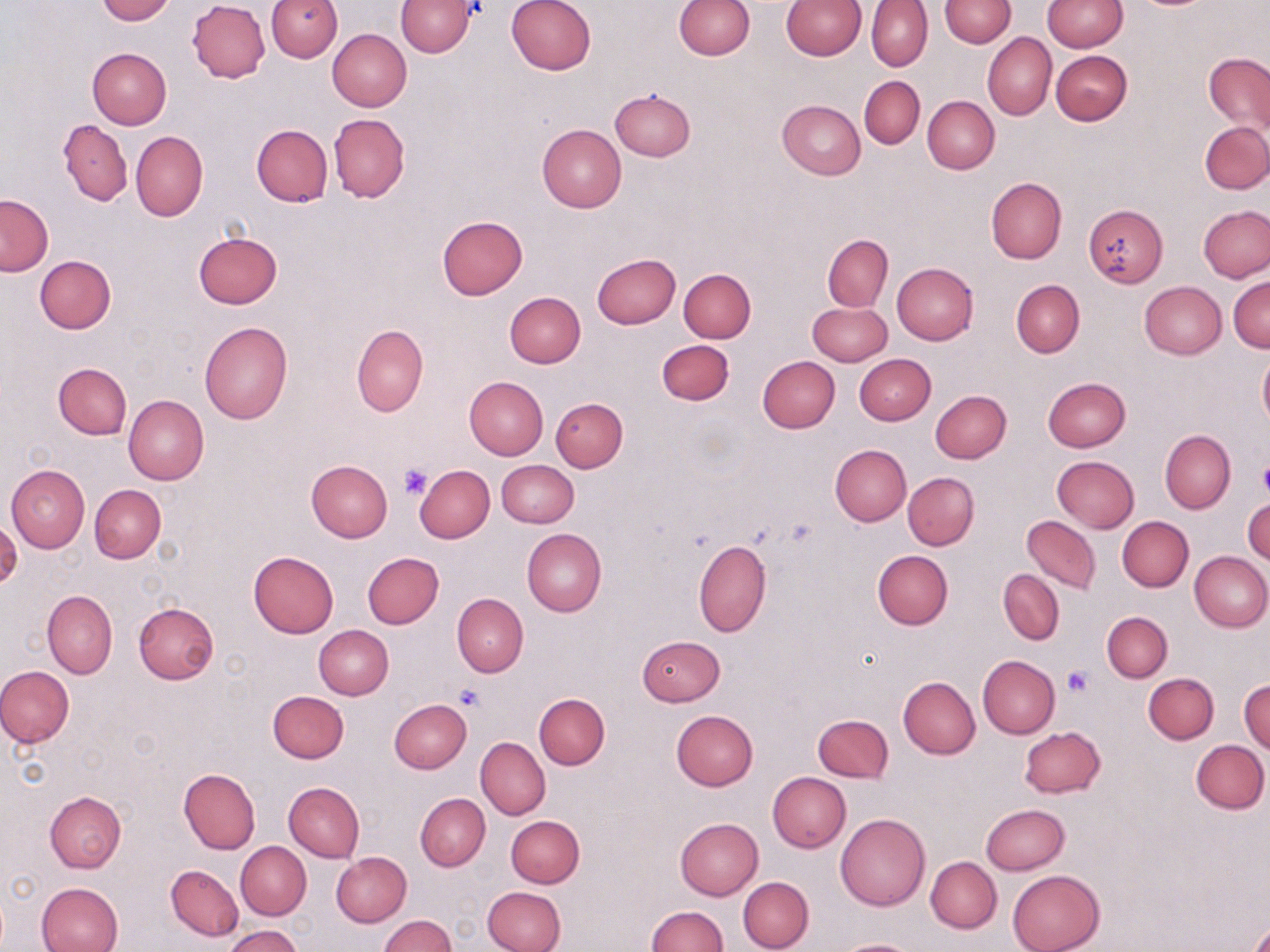

Approximate bounding boxes as (x1, y1, x2, y2) in pixels. Platelet locations: (1257, 459, 1270, 497), (399, 462, 433, 499), (1063, 664, 1094, 696), (455, 684, 485, 711). Uninfected red blood cell locations: (96, 0, 173, 24), (266, 0, 342, 62), (505, 0, 596, 75), (674, 0, 754, 59), (781, 0, 864, 59), (939, 0, 1015, 47), (1041, 0, 1128, 51), (187, 1, 270, 82), (397, 1, 475, 57), (867, 1, 932, 71), (327, 28, 411, 111), (983, 32, 1056, 119), (88, 48, 171, 128), (1051, 50, 1132, 126), (1204, 53, 1270, 134), (859, 76, 924, 149), (610, 88, 695, 161), (923, 95, 999, 174), (777, 99, 865, 179), (329, 114, 410, 202), (58, 119, 131, 206), (1201, 122, 1270, 193), (251, 123, 333, 206), (537, 123, 627, 212), (131, 131, 208, 220), (986, 177, 1067, 263), (0, 194, 53, 276), (1082, 204, 1167, 287), (1197, 205, 1270, 283), (437, 215, 527, 299), (193, 231, 283, 309), (823, 235, 892, 311), (593, 253, 680, 328), (35, 256, 116, 334), (892, 262, 978, 344), (679, 269, 755, 342), (1228, 275, 1269, 352), (1011, 280, 1083, 355), (1140, 281, 1226, 360), (504, 291, 585, 368), (807, 302, 891, 366), (199, 321, 294, 424), (352, 324, 428, 415), (656, 340, 734, 405), (1257, 353, 1270, 431), (853, 354, 935, 424), (757, 356, 840, 433), (53, 363, 132, 439), (464, 376, 548, 460), (1042, 377, 1131, 451), (931, 390, 1012, 463), (124, 395, 209, 485), (551, 397, 629, 472), (1160, 430, 1235, 513), (829, 445, 910, 526), (1052, 456, 1139, 532), (497, 460, 579, 527), (306, 461, 393, 542), (414, 464, 495, 543), (5, 465, 90, 551), (902, 472, 980, 551), (90, 484, 165, 563), (1243, 498, 1270, 565), (1021, 515, 1100, 593), (1117, 515, 1193, 592), (522, 529, 606, 618), (694, 540, 771, 637), (873, 550, 953, 629), (1189, 550, 1270, 631), (249, 551, 338, 638), (362, 552, 444, 628), (999, 569, 1064, 644), (43, 591, 117, 677), (452, 594, 528, 676), (132, 602, 220, 684), (1102, 611, 1172, 682), (313, 624, 393, 699), (638, 635, 725, 706), (978, 655, 1060, 738), (0, 665, 74, 748), (1144, 673, 1218, 744), (899, 677, 980, 759), (1239, 679, 1269, 754), (267, 690, 348, 763), (535, 693, 609, 769), (389, 699, 471, 774), (670, 711, 758, 790), (813, 715, 893, 783), (1020, 725, 1106, 798), (476, 737, 550, 820), (1191, 739, 1269, 814), (178, 768, 259, 853), (767, 772, 851, 853), (284, 782, 364, 862), (44, 790, 127, 873), (415, 793, 490, 870), (980, 804, 1069, 875), (836, 813, 931, 910), (505, 815, 584, 888), (675, 817, 763, 899), (235, 842, 311, 919), (331, 851, 412, 926), (926, 857, 1001, 933), (166, 864, 242, 940), (1007, 869, 1105, 952), (738, 877, 814, 952), (36, 881, 124, 952), (483, 885, 567, 952), (646, 905, 728, 952), (378, 915, 455, 952), (1249, 922, 1270, 952), (225, 925, 302, 952), (835, 938, 920, 952). Slide-level diagnosis: no evidence of blood parasites. One field of a larger specimen. Optical microscopy. Captured at 1000x magnification. Image is 1270×952 pixels. May-Grünwald-Giemsa-stained preparation. Thin blood film.